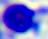

modality: micrograph
magnification: 400x
identification: white blood cell